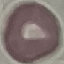

{
  "result": "no malaria parasites seen",
  "preparation": "thin blood smear",
  "stain": "Giemsa",
  "image_type": "automatically extracted cell patch, resized to 64 × 64 pixels",
  "capture": "smartphone camera at the microscope eyepiece"
}